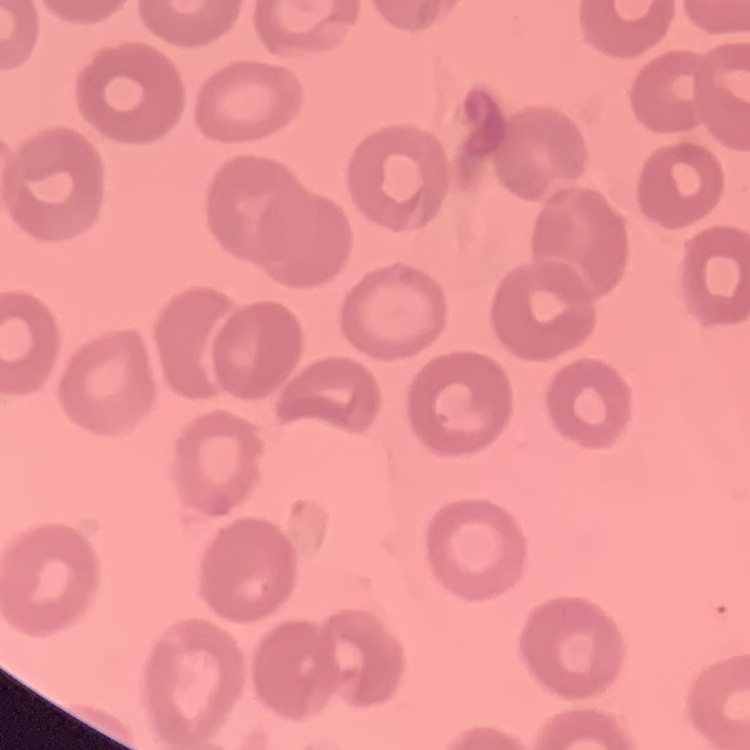

The red blood cells exhibit no rouleaux formation. Thin blood film. One tile cut from a larger photomicrograph. Field's or Giemsa stain.